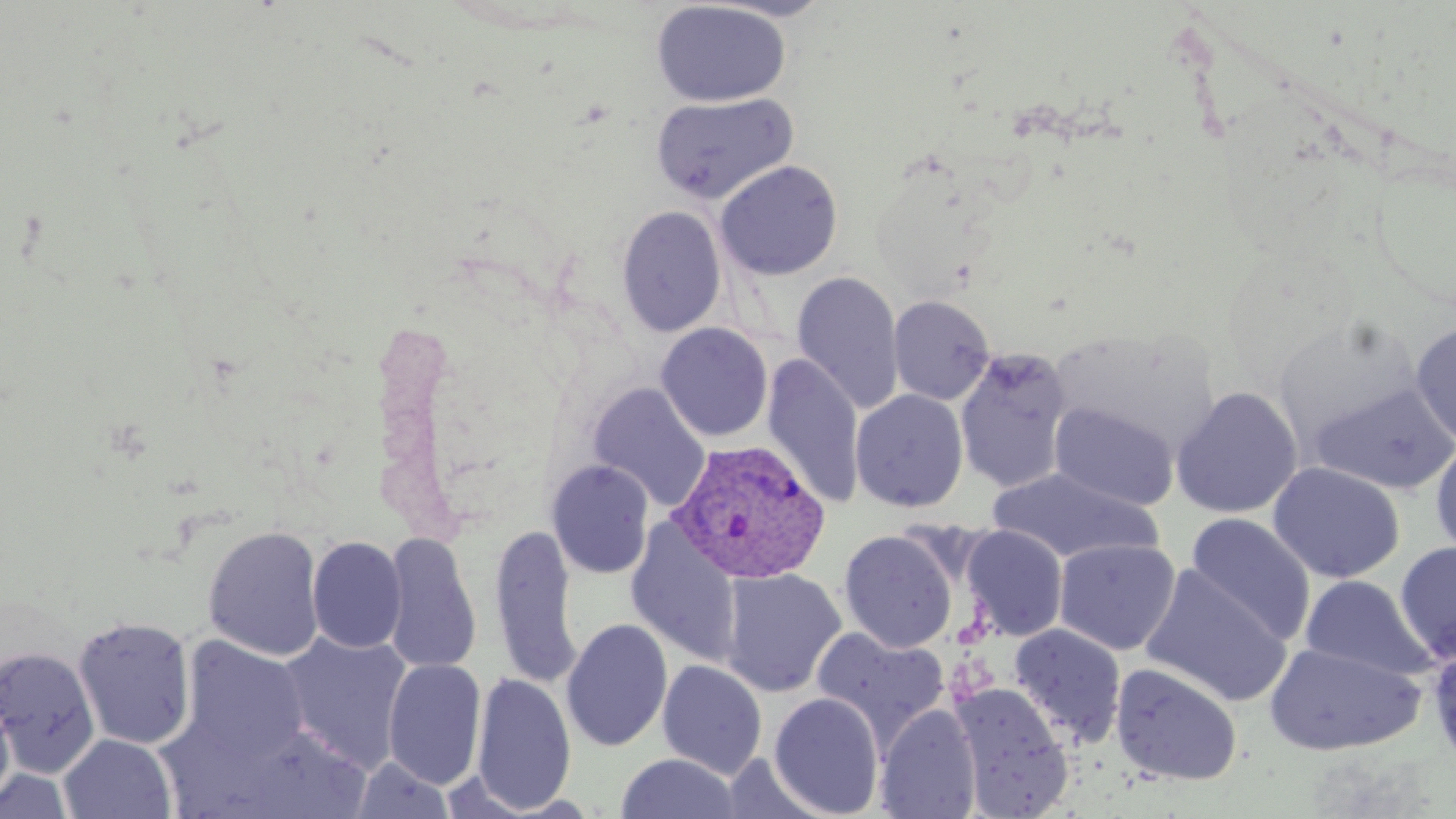 Approximate bounding boxes as [x1, y1, x2, y2] in pixels. Uninfected red blood cell locations: [651, 1, 791, 107], [650, 93, 797, 205], [715, 160, 843, 280], [616, 206, 726, 338], [791, 271, 904, 415], [889, 296, 995, 405], [1273, 313, 1423, 449], [1410, 321, 1456, 447], [655, 323, 773, 442], [1051, 329, 1219, 456], [954, 348, 1073, 495], [762, 354, 865, 509], [1310, 381, 1456, 494], [588, 383, 711, 511], [1171, 386, 1303, 519], [850, 389, 969, 513], [1049, 401, 1178, 510], [1430, 439, 1456, 563], [546, 460, 655, 580], [1267, 461, 1405, 583], [986, 467, 1163, 565], [1184, 513, 1316, 646], [489, 523, 583, 690], [626, 523, 743, 668], [203, 525, 325, 661], [961, 525, 1068, 642], [839, 529, 958, 653], [380, 533, 482, 675], [307, 536, 406, 653], [1054, 538, 1181, 655], [1395, 541, 1456, 664], [1139, 564, 1293, 707], [720, 568, 846, 698], [1299, 574, 1435, 682], [72, 615, 197, 750], [561, 619, 673, 752], [1008, 624, 1127, 746], [811, 626, 951, 750], [277, 631, 413, 772], [179, 636, 310, 765], [1263, 641, 1423, 756], [0, 646, 100, 777], [383, 659, 486, 789], [658, 660, 767, 779], [1110, 662, 1243, 786], [470, 672, 577, 813], [949, 682, 1074, 817], [0, 687, 16, 811], [768, 692, 885, 818], [875, 703, 981, 819], [227, 724, 372, 819], [59, 734, 177, 818], [615, 753, 743, 818], [351, 756, 455, 819], [0, 769, 75, 818]. Plasmodium vivax-infected red blood cell locations: [669, 439, 832, 586]. Slide-level diagnosis: Plasmodium vivax. Image is 1456×819 pixels. Single field of view. Captured at 1000x magnification. Light microscopy. Thin blood smear. May-Grünwald-Giemsa-stained preparation.